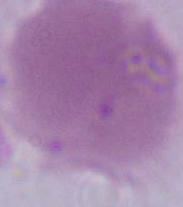 Photomicrograph. Captured at 1000x magnification. A red blood cell is shown.